Name the parasite shown.
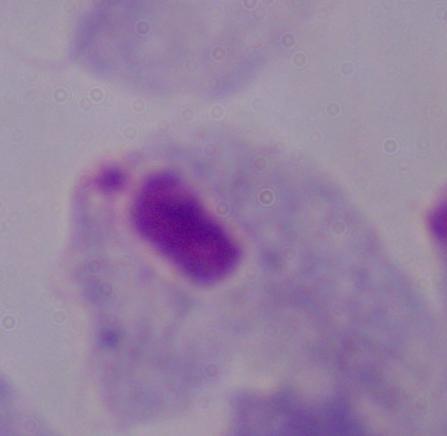
A trichomonad.

modality = micrograph
magnification = 1000x